Point out each malaria parasite.
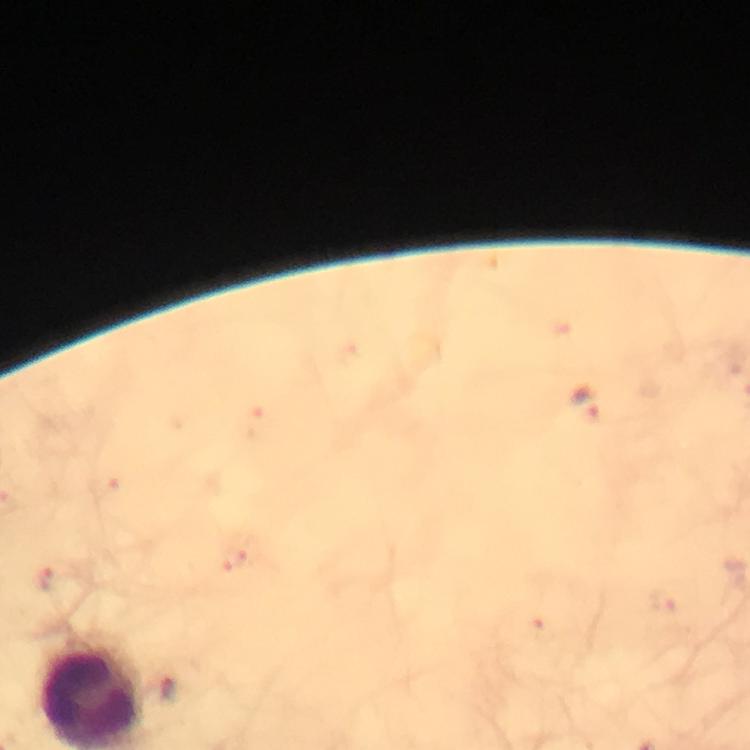

Approximate centers as {x, y} in pixels.
Malaria parasites: {587, 406}.

stain = Giemsa
context = from a malaria diagnostic workup
preparation = thick smear
immersion oil = used
cropped from = one field of view
capture = smartphone photograph through a microscope
magnification = 100x
image size = 750×750 pixels